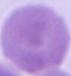
Summary:
  - Modality: micrograph
  - Identification: red blood cell
  - Magnification: 1000x